Name the parasite shown.
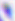

Toxoplasma gondii.

400x magnification. Micrograph.